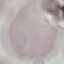

Malaria status: uninfected. Automatically extracted cell patch, resized to 64 × 64 pixels. Thin blood smear. Giemsa-stained preparation. Photographed with a smartphone camera at the microscope eyepiece.